Describe the morphology of the erythrocytes.
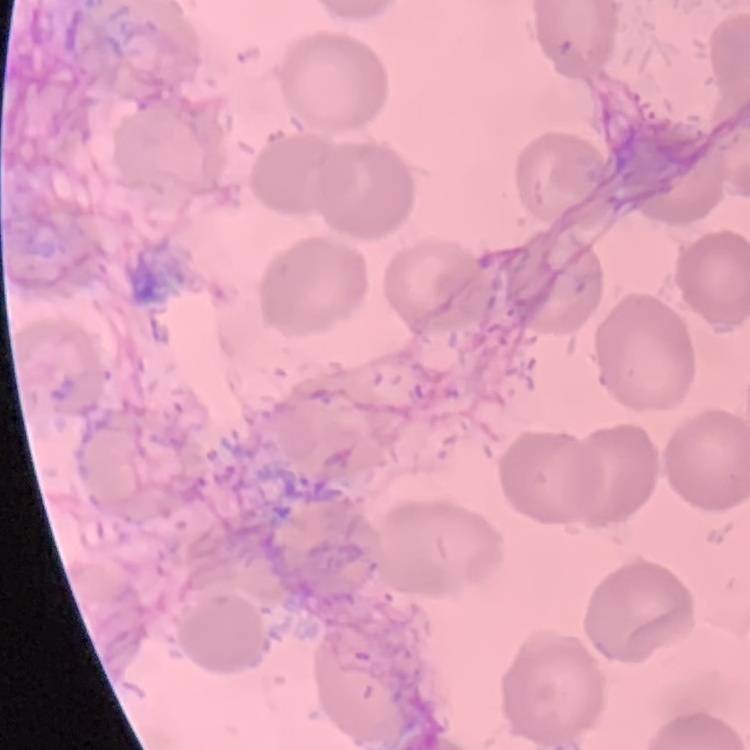
They show no rouleaux formation.

Summary:
  - Preparation: thin blood smear
  - Stain: Field's or Giemsa
  - Image type: one tile cut from a larger photomicrograph